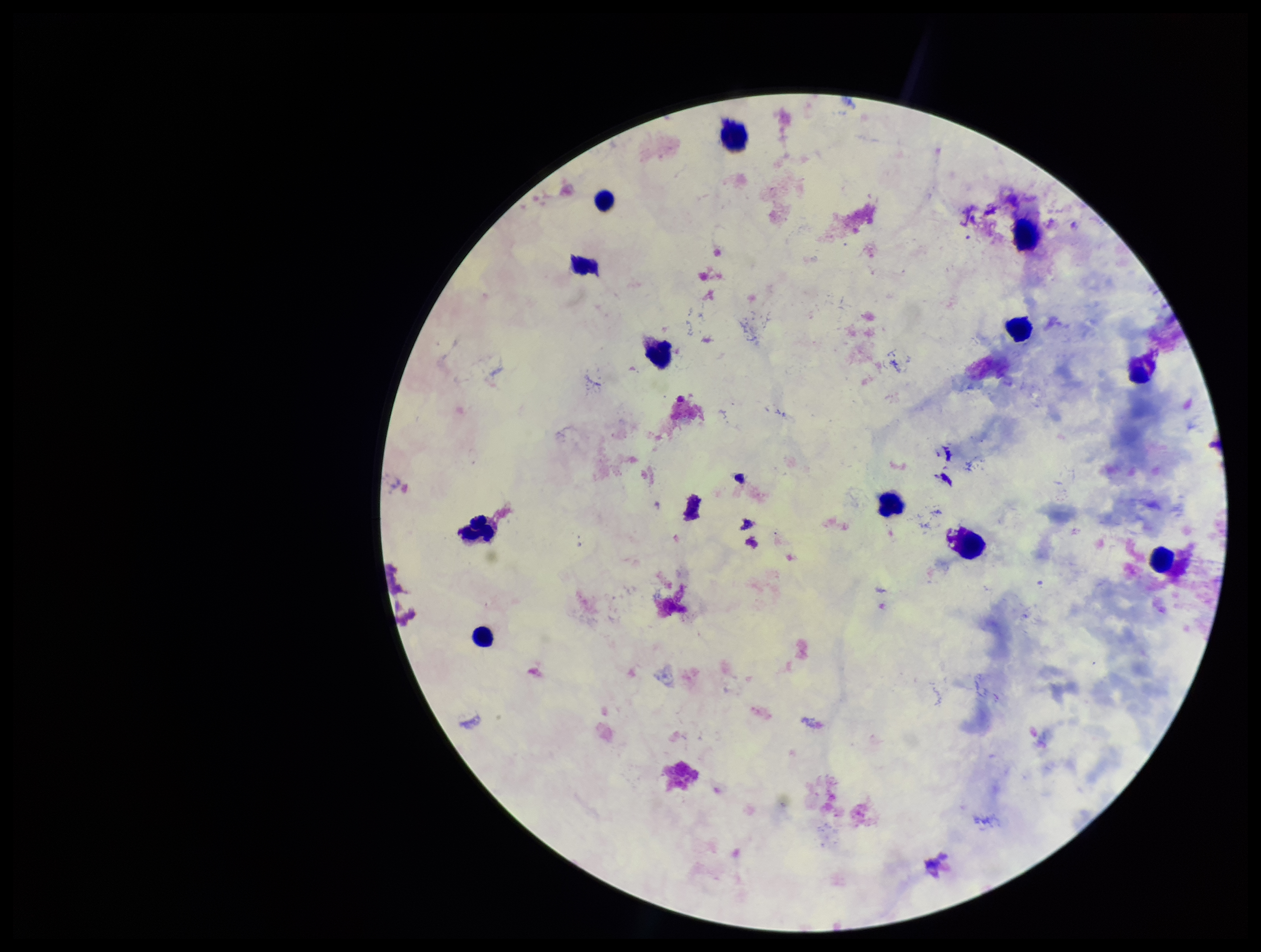

Summary:
  - Parasite count: 0
  - Leukocyte count: 12
  - Stain: Giemsa
  - Image size: 1261×952 pixels
  - Field of view: single
  - Capture: smartphone photograph through the microscope eyepiece
  - Plasmodium parasites: none identified
  - Preparation: thick
  - Patient malaria status: negative